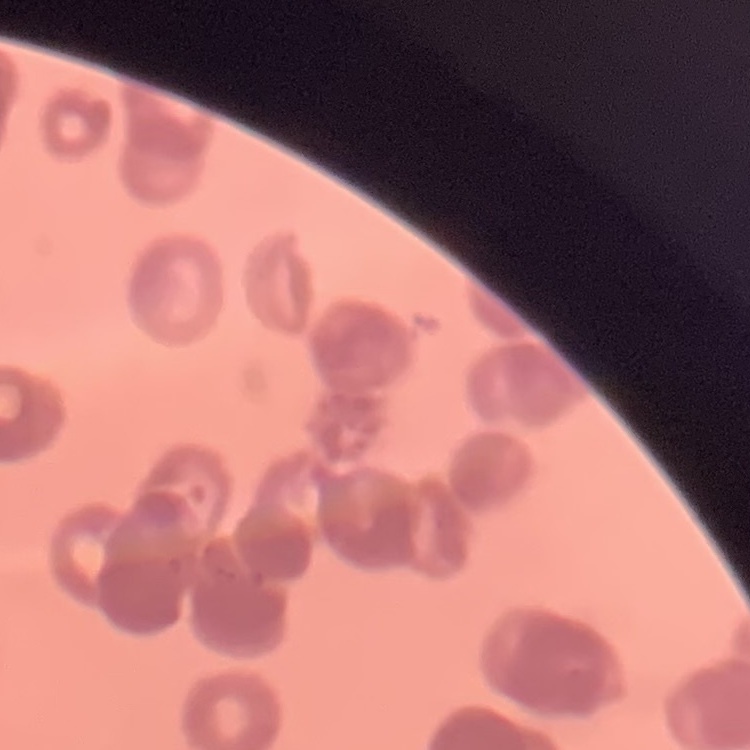
The red blood cells show rouleaux formation. One tile cut from a larger photomicrograph. Stained with either Field's or Giemsa. Thin blood film.